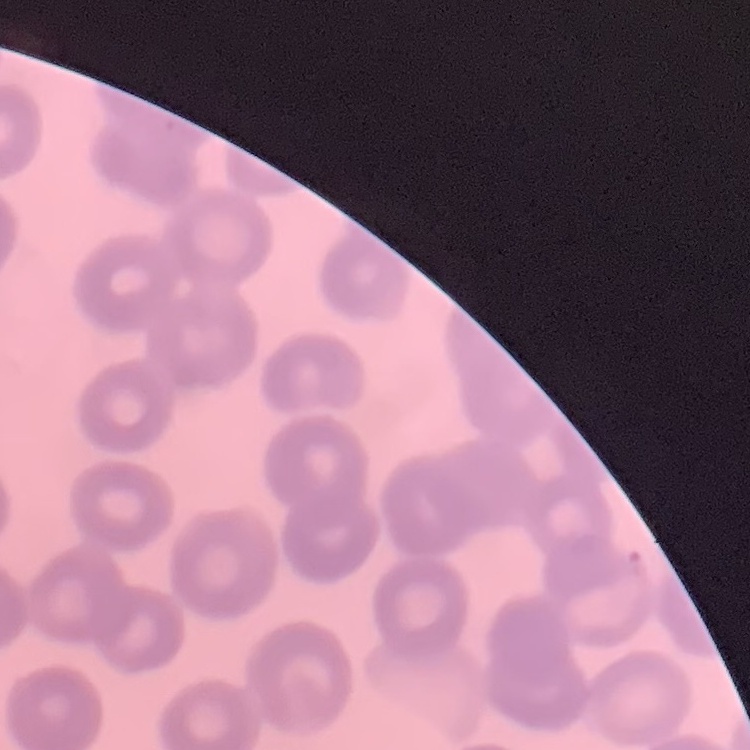

red blood cell morphology = no rouleaux formation
preparation = thin peripheral smear
stain = Field's or Giemsa
image type = square crop of a larger photomicrograph